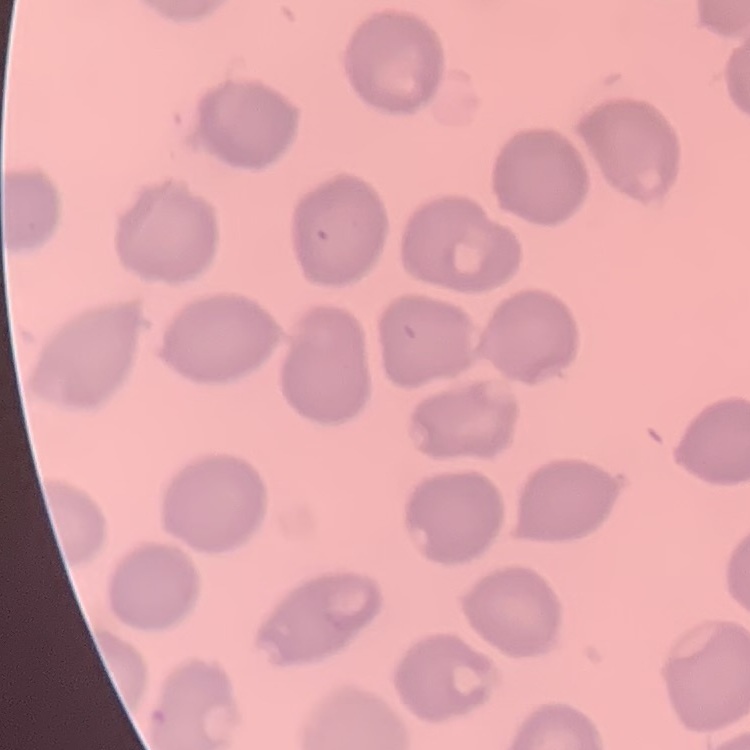 The red blood cells exhibit no rouleaux formation. Stained with either Field's or Giemsa. Thin peripheral smear. One tile cut from a larger photomicrograph.